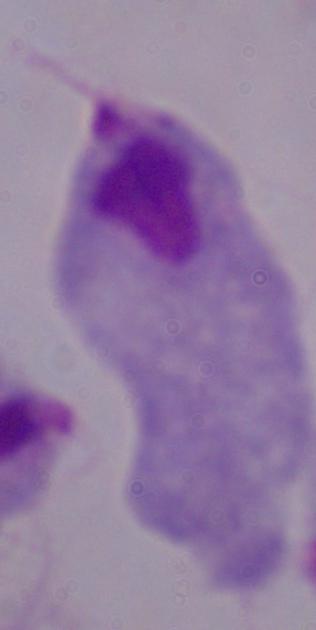
identification = trichomonad
magnification = 1000x
modality = micrograph